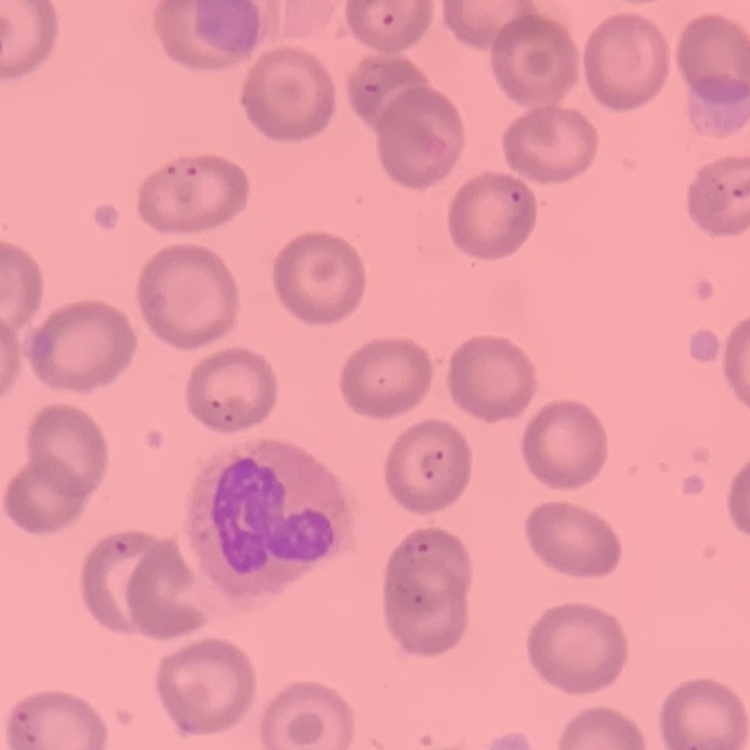

red blood cell morphology = no rouleaux formation
stain = Field's or Giemsa
image type = square crop of a larger photomicrograph
preparation = thin blood film